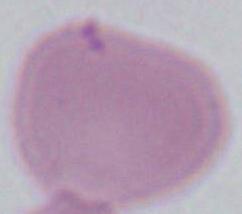 A red blood cell is shown. Micrograph. 1000x magnification.